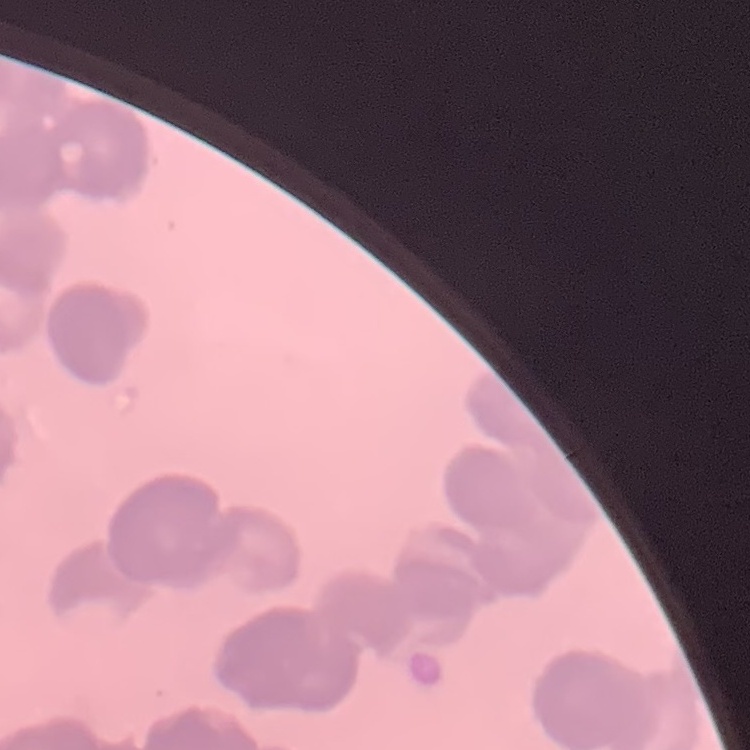
The erythrocytes exhibit rouleaux formation. Thin blood smear. One tile cut from a larger photomicrograph. Stained with either Field's or Giemsa.